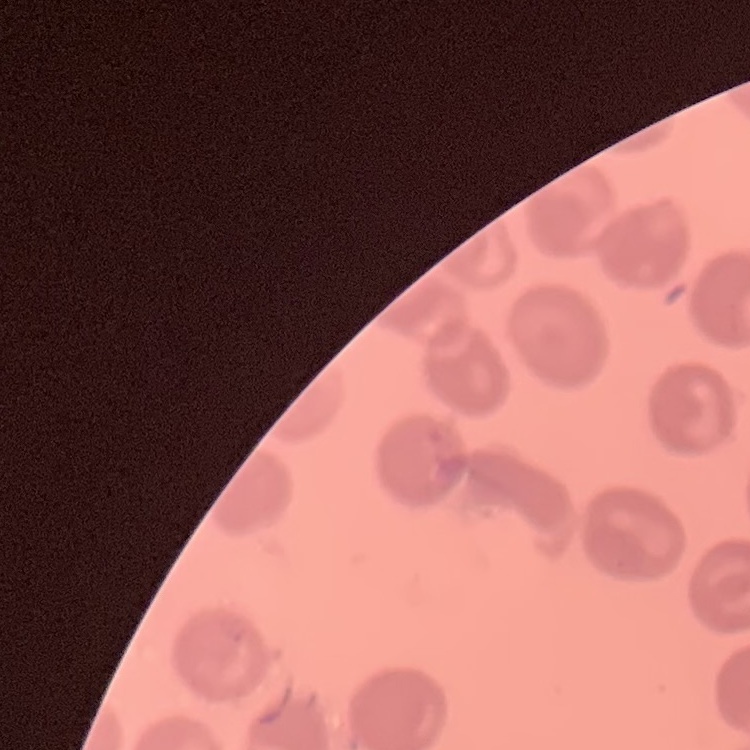
The red blood cells exhibit no rouleaux formation. Field's or Giemsa stain. Thin blood smear. One tile cut from a larger photomicrograph.